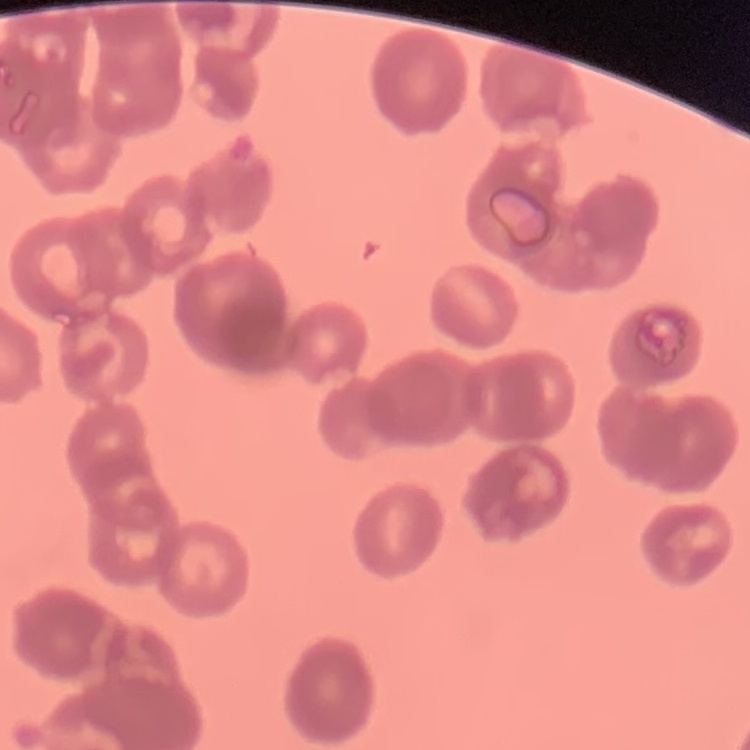
The erythrocytes exhibit rouleaux formation. Square crop of a larger photomicrograph. Thin blood smear. Stained with either Field's or Giemsa.